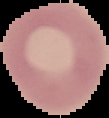

Summary:
  - Result: no malaria parasites seen
  - Image type: cell region segmented out of the field of view; surrounding area masked to black
  - Image size: 109×118 pixels
  - Preparation: thin blood smear